Mark where platelets are.
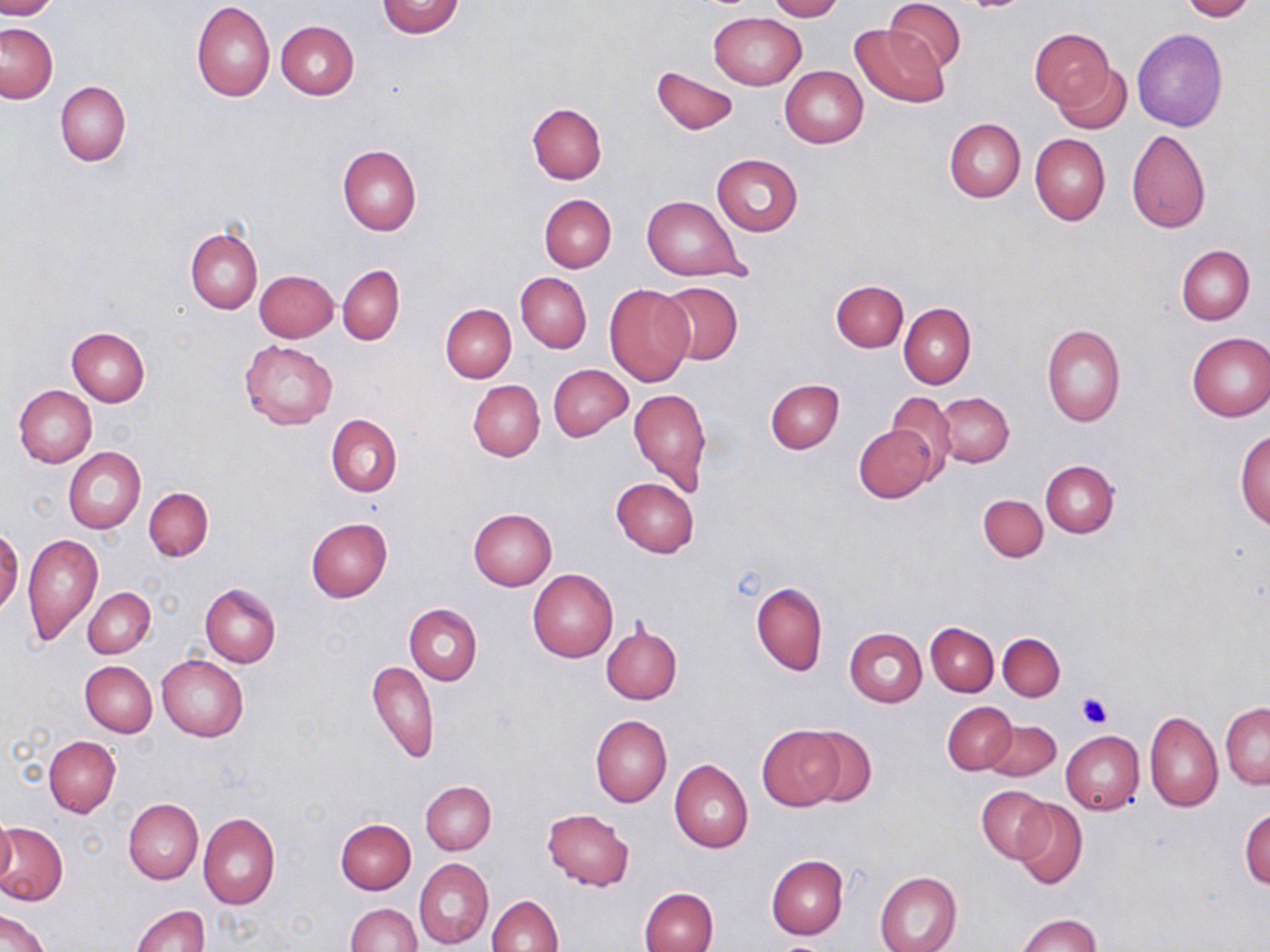

Approximate bounding boxes as (x1, y1, x2, y2) in pixels.
Platelets: (1076, 692, 1113, 729).

slide-level diagnosis = no evidence of blood parasites
uninfected red blood cell locations = approximate bounding boxes as (x1, y1, x2, y2) in pixels: (0, 0, 58, 19), (767, 0, 843, 21), (884, 0, 966, 73), (1178, 0, 1256, 21), (375, 1, 467, 38), (192, 3, 275, 101), (709, 12, 806, 90), (276, 21, 359, 99), (0, 23, 57, 103), (851, 24, 950, 107), (1029, 27, 1115, 110), (1131, 28, 1227, 132), (1054, 62, 1133, 133), (653, 65, 737, 135), (780, 66, 868, 148), (55, 82, 130, 165), (527, 103, 607, 185), (944, 118, 1026, 202), (1126, 128, 1211, 234), (1029, 133, 1110, 225), (337, 144, 421, 235), (711, 154, 803, 235), (540, 194, 616, 272), (642, 196, 749, 282), (186, 226, 262, 314), (1177, 244, 1254, 324), (338, 265, 404, 345), (255, 270, 338, 342), (516, 272, 591, 352), (831, 279, 908, 351), (657, 281, 743, 365), (605, 284, 695, 386), (900, 303, 975, 389), (440, 304, 516, 382), (1041, 325, 1126, 427), (67, 328, 149, 407), (1185, 332, 1270, 421), (240, 340, 338, 430), (549, 364, 633, 441), (765, 378, 844, 453), (468, 379, 545, 462), (13, 385, 97, 468), (629, 388, 711, 496), (887, 391, 955, 474), (934, 392, 1014, 468), (326, 413, 403, 497), (854, 426, 937, 502), (1234, 428, 1270, 531), (64, 447, 145, 533), (1040, 460, 1118, 537), (611, 478, 699, 557), (144, 488, 213, 562), (978, 495, 1047, 561), (468, 509, 556, 591), (305, 518, 392, 602), (1, 526, 21, 617), (22, 533, 104, 647), (529, 569, 618, 662), (751, 582, 828, 675), (201, 585, 281, 666), (83, 587, 155, 659), (404, 604, 482, 686), (600, 622, 682, 704), (926, 622, 999, 695), (844, 629, 926, 707), (998, 632, 1066, 700), (156, 655, 248, 741), (367, 659, 439, 763), (80, 660, 157, 737), (943, 702, 1016, 774), (1221, 703, 1270, 788), (1145, 711, 1222, 811), (590, 714, 671, 808), (983, 719, 1061, 781), (758, 725, 844, 809), (798, 725, 876, 806), (1061, 731, 1144, 815), (45, 736, 121, 817), (670, 759, 753, 852), (420, 781, 495, 854), (976, 785, 1053, 863), (124, 798, 203, 884), (1012, 798, 1086, 889), (1240, 808, 1270, 890), (542, 809, 635, 890), (198, 812, 280, 908), (0, 813, 17, 891), (336, 818, 416, 893), (0, 822, 68, 906), (766, 855, 847, 940), (414, 858, 494, 949), (874, 871, 962, 952), (639, 887, 718, 952), (487, 894, 563, 952), (346, 903, 422, 952), (130, 905, 209, 952), (0, 909, 51, 952), (1014, 913, 1100, 952)
stain = May-Grünwald-Giemsa
magnification = 1000x
image size = 1270×952 pixels
preparation = thin blood smear
modality = light microscopy
field of view = single